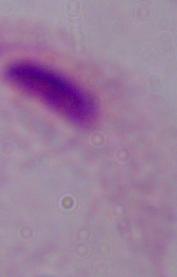

Summary:
  - Magnification: 1000x
  - Identification: trichomonad
  - Modality: micrograph